State which parasite is depicted.
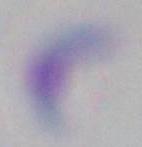

This is Toxoplasma gondii.

Captured at 1000x magnification. Photomicrograph.